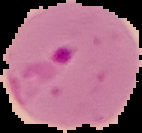
{
  "result": "malaria parasites detected",
  "image_type": "segmented cell region with the area outside set to black",
  "preparation": "thin blood smear",
  "image_size": "142×133 pixels"
}